Report the malaria status of this cell.
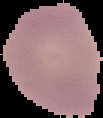
It is uninfected.

image type = segmented cell region with the area outside set to black
image size = 103×118 pixels
preparation = thin blood smear